Identify the parasite.
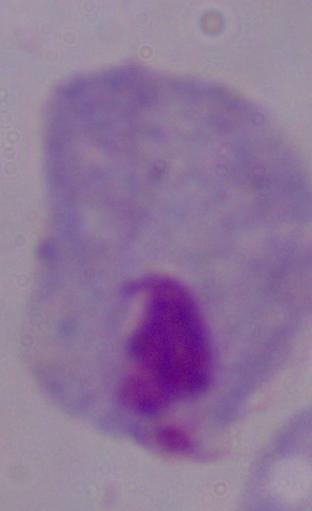
A trichomonad.

Summary:
  - Magnification: 1000x
  - Modality: photomicrograph